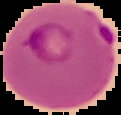

Image is 121×115 pixels. Segmented cell region on a black background. Malaria status: parasitized. From a thin blood smear.